Report the malaria status of this cell.
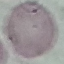

Uninfected.

Summary:
  - Image type: automatically extracted cell patch, resized to 64 × 64 pixels
  - Preparation: thin smear
  - Stain: Giemsa
  - Capture: smartphone camera at the microscope eyepiece